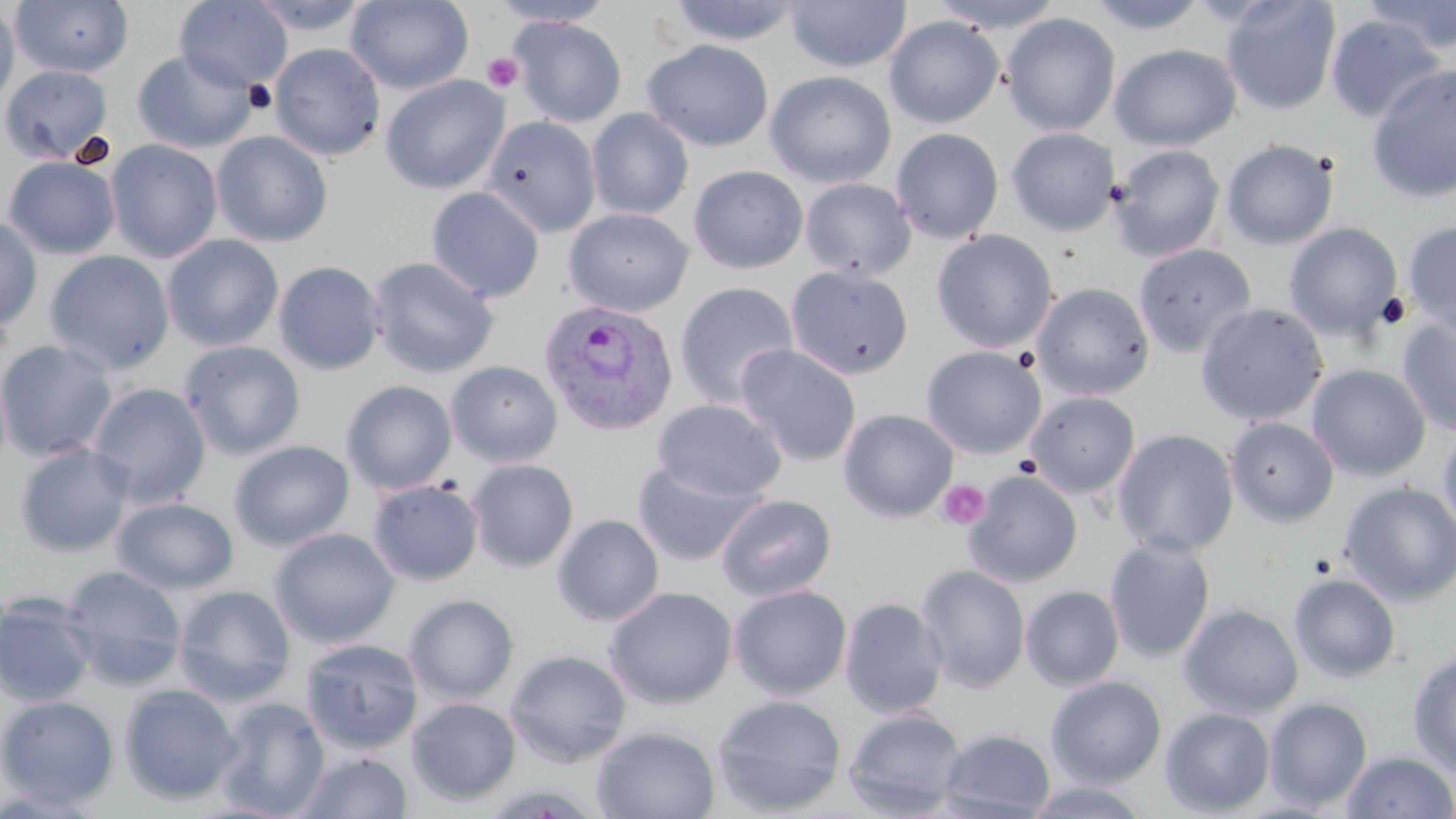
Plasmodium vivax-infected red blood cell locations = approximate bounding boxes as (x1,y1)-(x2,y2) corner pairs in pixels: (538,298)-(677,437)
slide-level diagnosis = Plasmodium vivax
uninfected red blood cell locations = approximate bounding boxes as (x1,y1)-(x2,y2) corner pairs in pixels: (11,0)-(134,77), (174,0)-(293,93), (247,0)-(372,35), (346,0)-(474,94), (668,0)-(803,46), (785,0)-(910,72), (929,0)-(1066,33), (1085,0)-(1210,34), (1221,0)-(1342,115), (1361,0)-(1456,54), (489,1)-(616,26), (0,2)-(19,111), (1001,13)-(1121,136), (1326,15)-(1445,123), (510,16)-(627,127), (884,16)-(1004,128), (642,39)-(774,152), (269,43)-(386,161), (1110,43)-(1241,151), (132,50)-(257,153), (1,65)-(113,164), (1366,65)-(1456,202), (765,71)-(897,188), (381,75)-(509,194), (587,108)-(694,220), (481,115)-(601,237), (891,128)-(1004,244), (1006,128)-(1120,236), (212,131)-(334,247), (104,139)-(223,263), (1221,139)-(1339,250), (1110,145)-(1226,261), (3,155)-(121,259), (688,165)-(809,273), (800,178)-(917,281), (426,187)-(545,304), (564,208)-(693,317), (0,214)-(43,332), (1403,221)-(1456,338), (1284,223)-(1403,339), (932,230)-(1057,353), (162,235)-(283,352), (1133,242)-(1257,358), (44,251)-(174,374), (367,256)-(500,378), (273,260)-(385,375), (786,265)-(914,380), (675,282)-(799,410), (1031,283)-(1154,400), (1195,303)-(1328,425), (1397,315)-(1456,438), (0,340)-(118,461), (180,340)-(305,460), (735,344)-(861,466), (921,346)-(1047,459), (446,360)-(563,467), (1306,364)-(1431,482), (341,380)-(457,495), (87,383)-(211,508), (1026,391)-(1140,498), (653,399)-(786,502), (839,408)-(958,522), (1225,417)-(1339,527), (1439,424)-(1456,544), (1112,429)-(1240,557), (229,440)-(355,552), (15,443)-(135,558), (246,444)-(374,634), (467,459)-(579,571), (631,460)-(764,566), (965,470)-(1083,587), (368,479)-(483,585), (1339,481)-(1456,605), (716,494)-(837,601), (111,497)-(239,594), (552,514)-(664,626), (269,528)-(399,648), (1103,536)-(1216,663), (916,565)-(1031,692), (60,566)-(187,690), (1289,573)-(1402,682), (173,585)-(296,706), (728,585)-(852,700), (1021,585)-(1125,690), (604,586)-(738,709), (1,590)-(97,708), (405,594)-(520,704), (840,597)-(948,718), (1178,604)-(1303,718), (299,638)-(423,755), (505,649)-(632,767), (1408,652)-(1456,777), (1046,676)-(1167,788), (118,683)-(242,805), (712,694)-(848,816), (0,695)-(119,809), (214,696)-(330,817), (407,698)-(521,806), (1264,698)-(1373,810), (843,707)-(967,816), (1160,707)-(1275,816), (591,725)-(721,819), (938,728)-(1055,819), (295,751)-(413,818), (1341,751)-(1455,818), (1021,779)-(1155,818)
field of view = one of a larger specimen
stain = May-Grünwald-Giemsa
image size = 1456×819 pixels
platelet locations = approximate bounding boxes as (x1,y1)-(x2,y2) corner pairs in pixels: (482,52)-(524,94), (938,480)-(990,530)
modality = light microscopy
magnification = 1000x
preparation = thin blood smear